Give the position of every leukocyte visible.
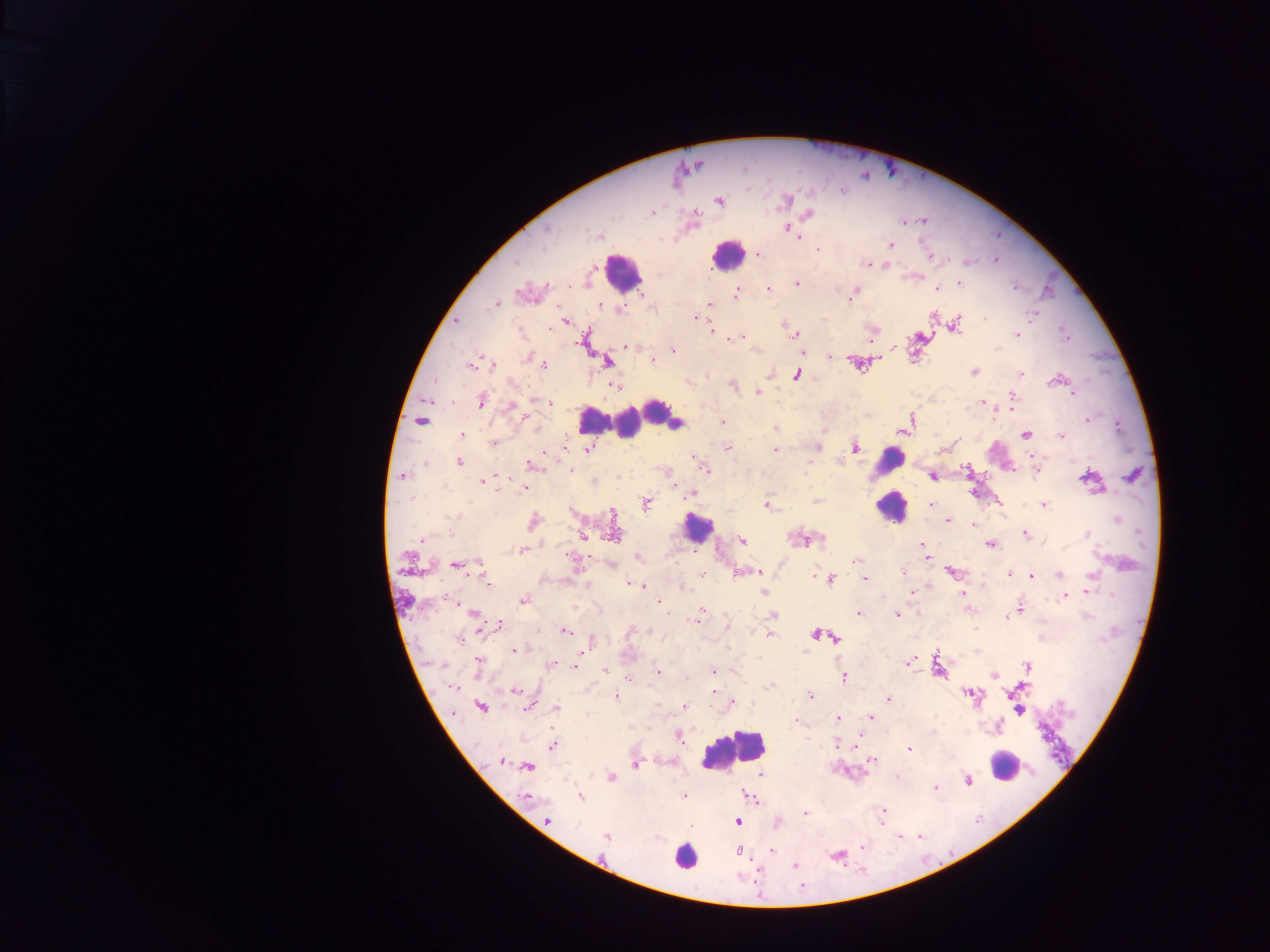
Approximate centers as {x, y} in pixels.
Leukocytes: {727, 254}, {622, 271}, {658, 410}, {592, 420}, {627, 423}, {888, 460}, {891, 508}, {697, 528}, {732, 750}, {1004, 765}, {685, 855}.

Summary:
  - Malaria parasite locations: {719, 201}, {786, 201}, {652, 213}, {809, 215}, {694, 216}, {923, 221}, {546, 229}, {793, 233}, {599, 236}, {890, 245}, {817, 249}, {759, 254}, {931, 256}, {996, 259}, {515, 262}, {866, 264}, {885, 265}, {959, 283}, {797, 284}, {569, 285}, {1014, 287}, {937, 288}, {768, 289}, {737, 292}, {853, 294}, {710, 304}, {494, 305}, {600, 307}, {620, 308}, {695, 317}, {985, 318}, {457, 320}, {565, 322}, {957, 325}, {711, 330}, {1017, 334}, {793, 335}, {738, 338}, {871, 339}, {895, 346}, {627, 347}, {673, 350}, {527, 357}, {830, 357}, {606, 361}, {653, 361}, {470, 365}, {543, 365}, {492, 366}, {974, 371}, {1022, 373}, {770, 374}, {797, 374}, {1056, 380}, {733, 385}, {614, 386}, {758, 392}, {1074, 393}, {1012, 396}, {481, 401}, {536, 401}, {547, 402}, {982, 403}, {1012, 403}, {511, 407}, {911, 419}, {1087, 420}, {422, 421}, {722, 421}, {676, 424}, {775, 428}, {462, 435}, {1026, 435}, {1061, 436}, {493, 443}, {816, 447}, {855, 447}, {588, 449}, {727, 449}, {776, 449}, {941, 450}, {1033, 455}, {694, 457}, {840, 461}, {459, 462}, {530, 463}, {424, 464}, {571, 469}, {704, 469}, {1036, 471}, {403, 475}, {499, 476}, {933, 476}, {1087, 478}, {482, 481}, {593, 481}, {673, 485}, {524, 488}, {692, 494}, {647, 504}, {767, 505}, {1044, 505}, {931, 506}, {613, 513}, {451, 516}, {1117, 519}, {948, 521}, {533, 522}, {973, 525}, {1025, 534}, {1087, 534}, {613, 535}, {583, 536}, {421, 540}, {803, 540}, {742, 541}, {922, 544}, {990, 545}, {523, 550}, {638, 557}, {925, 557}, {855, 561}, {480, 563}, {455, 565}, {756, 571}, {950, 571}, {902, 573}, {1010, 574}, {1059, 575}, {815, 576}, {1032, 576}, {1091, 576}, {864, 578}, {830, 580}, {487, 583}, {632, 584}, {643, 587}, {1088, 590}, {764, 592}, {910, 592}, {963, 593}, {1065, 596}, {523, 601}, {659, 602}, {1019, 608}, {702, 611}, {859, 613}, {474, 615}, {897, 615}, {774, 616}, {1006, 617}, {697, 620}, {499, 625}, {565, 631}, {769, 634}, {815, 634}, {458, 639}, {837, 639}, {590, 643}, {515, 650}, {479, 661}, {907, 663}, {551, 665}, {1027, 666}, {576, 667}, {712, 670}, {606, 671}, {658, 672}, {994, 675}, {844, 677}, {628, 679}, {769, 687}, {453, 688}, {516, 690}, {714, 692}, {616, 696}, {811, 696}, {888, 699}, {733, 702}, {529, 706}, {684, 706}, {481, 707}, {557, 708}, {1019, 711}, {870, 717}, {838, 718}, {796, 721}, {552, 746}, {909, 749}, {872, 759}, {501, 762}, {635, 765}, {528, 766}, {761, 775}, {611, 777}, {967, 781}, {935, 788}, {684, 795}, {580, 796}, {527, 797}, {883, 811}, {805, 814}, {547, 819}, {738, 821}, {778, 823}, {691, 827}, {606, 838}, {862, 847}, {771, 850}, {739, 851}, {795, 866}
  - Country: Ghana
  - Field of view: single
  - Image size: 1270×952 pixels
  - Capture: mobile-phone photograph through a microscope
  - Preparation: thick blood film